Locate every Plasmodium falciparum parasite and give its life-cycle stage, and locate every leukocyte and any debris.
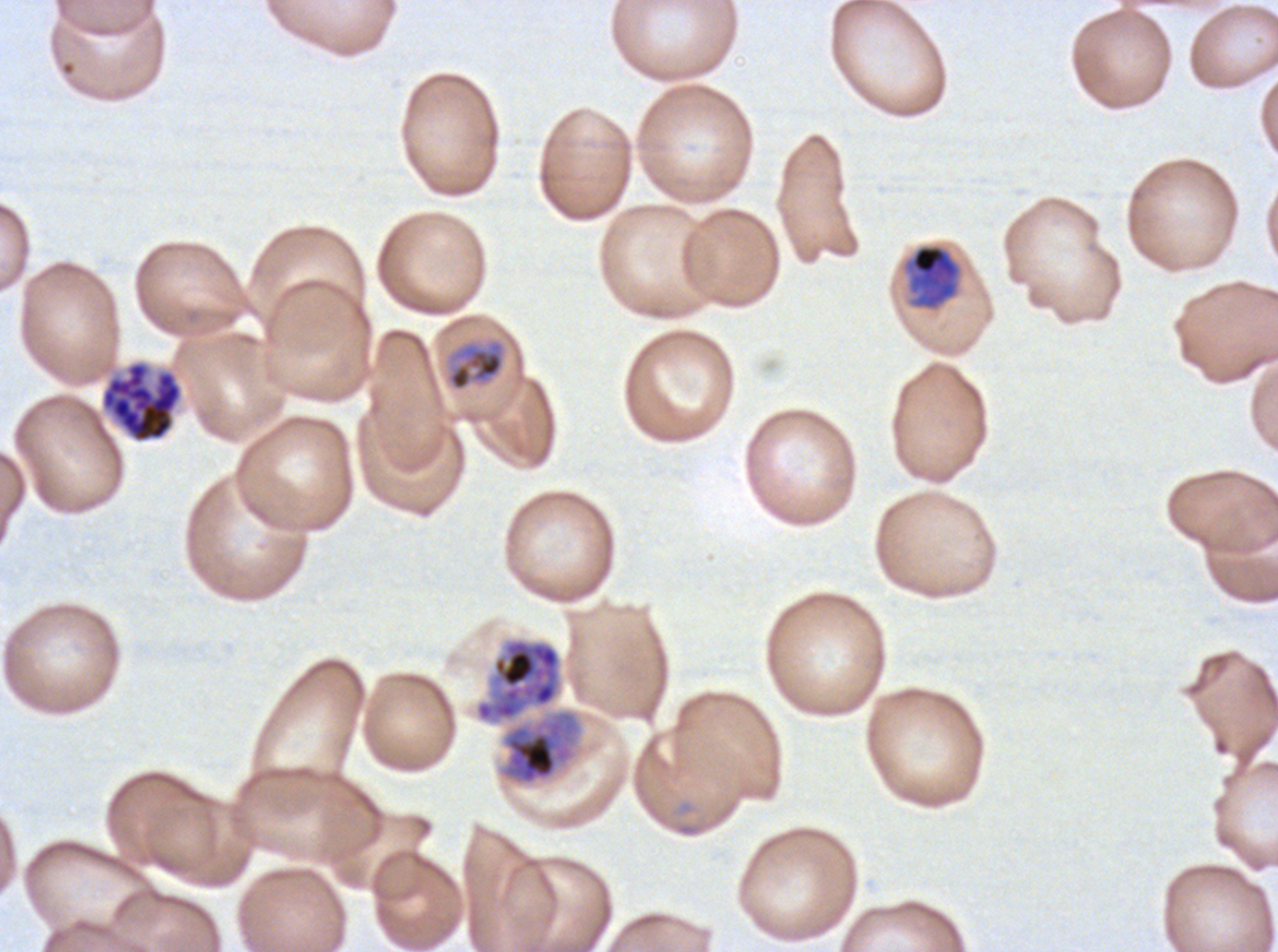

Approximate bounding boxes as {x1, y1, x2, y2} in pixels.
Mid trophozoites: {904, 243, 962, 311}, {445, 337, 507, 392}.
Late trophozoites: {473, 637, 582, 786}.
Segmenters: {99, 359, 184, 445}.
No rings, late-ring/early-trophozoite forms, early schizonts, late schizonts, gametocytes, leukocytes, or debris observed.

Summary:
  - Specimen: Plasmodium falciparum from a patient in The Gambia, cultured ex vivo for 24 to 48 hours
  - Field of view: one sub-image of a larger composite
  - Image size: 1278×952 pixels
  - Stain: Giemsa
  - Preparation: thin blood smear
  - Life-cycle stages observed: mid trophozoite, late trophozoite, segmenter